Assess for Plasmodium parasites.
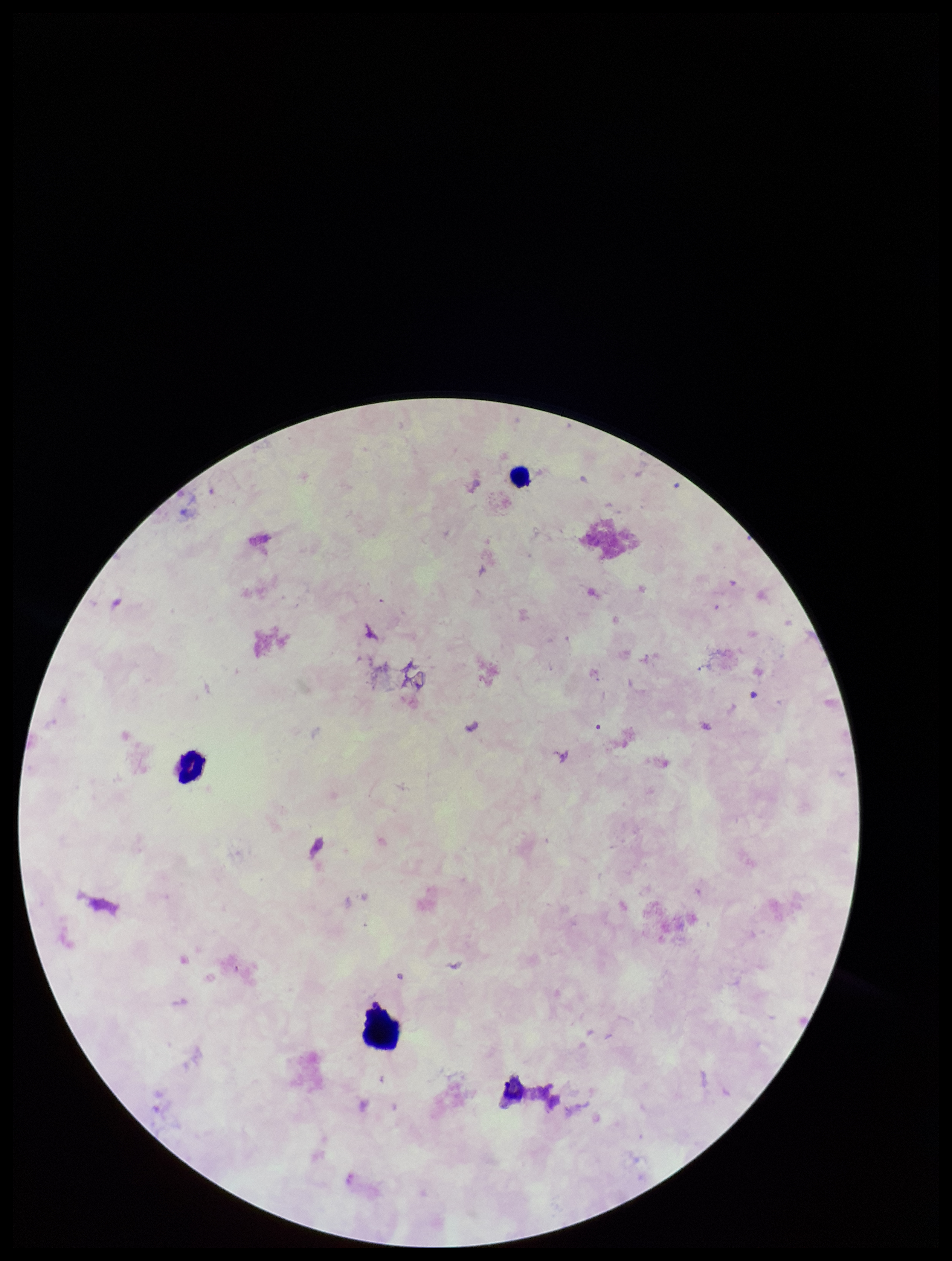
None detected.

capture = smartphone photograph through the microscope eyepiece
parasite count = 0
leukocyte count = 2
image size = 952×1261 pixels
stain = Giemsa
field of view = one from this slide
patient malaria status = negative
preparation = thick